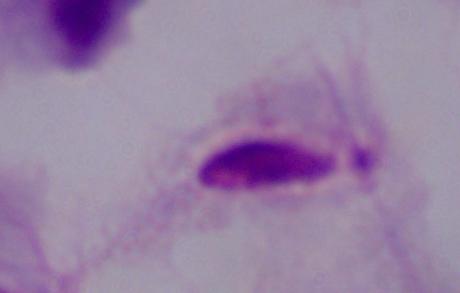
1000x magnification. Photomicrograph. A trichomonad is shown.